Give the preparation type.
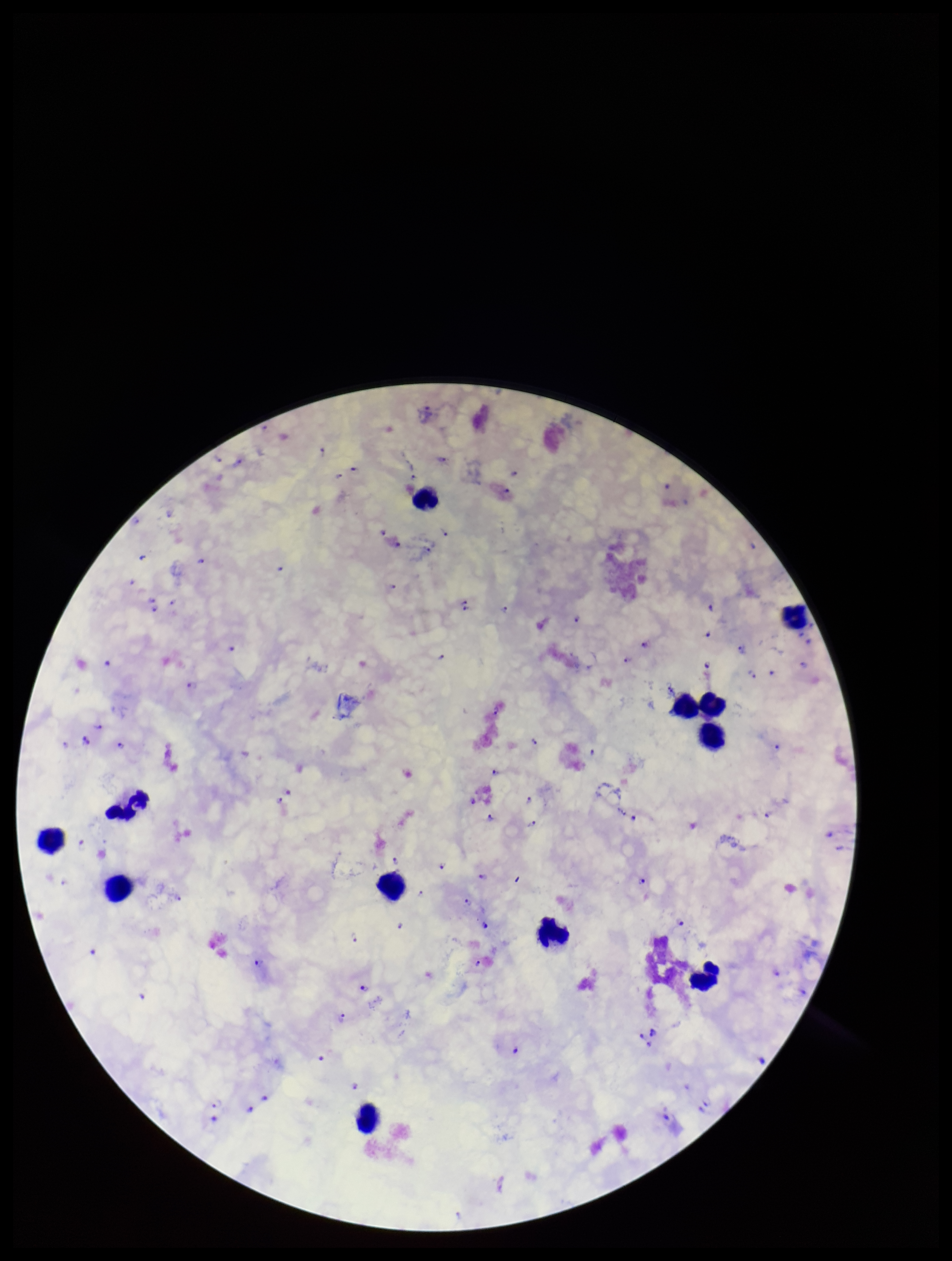

It is a thick blood smear.

Image is 952×1261 pixels. Single field of view. Patient malaria status: infected. Plasmodium parasites: detected. Parasite count: 98. Stained with Giemsa. Species reported for this patient: Plasmodium falciparum. Photographed through the microscope eyepiece with a smartphone camera. Leukocyte count: 12.